Describe the morphology of the red blood cells.
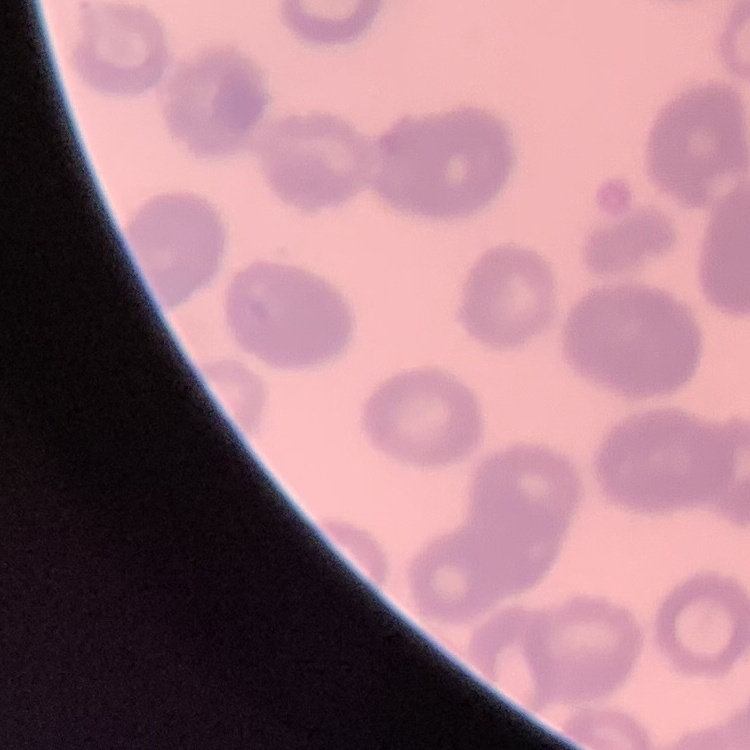
They show rouleaux formation.

Summary:
  - Preparation: thin blood smear
  - Image type: square crop of a larger photomicrograph
  - Stain: Field's or Giemsa